Locate every Plasmodium falciparum-infected red blood cell.
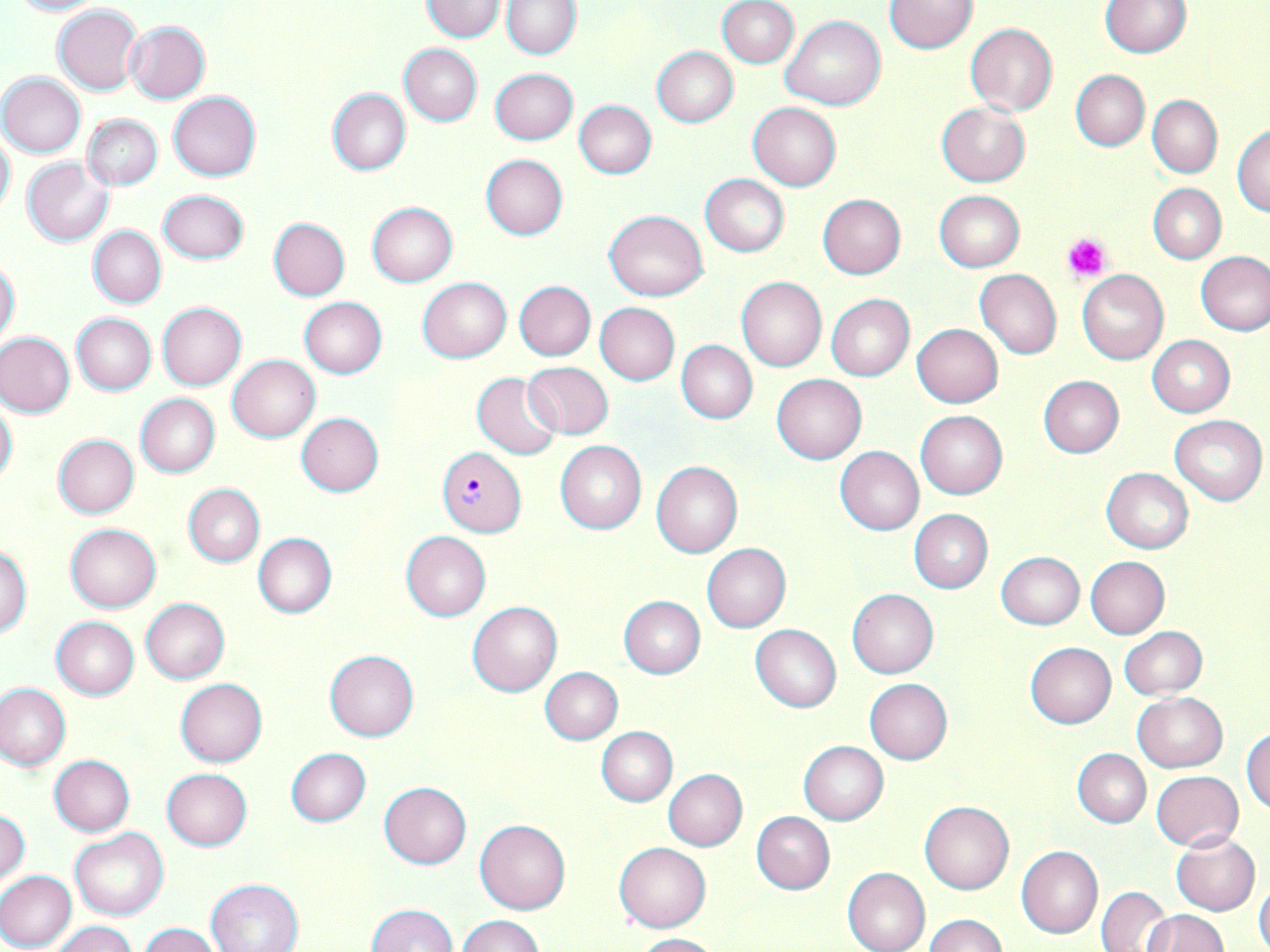
Approximate bounding boxes as (x1, y1, x2, y2) in pixels.
Plasmodium falciparum-infected red blood cells: (436, 447, 527, 535).

slide-level diagnosis = Plasmodium falciparum
stain = May-Grünwald-Giemsa
platelet locations = approximate bounding boxes as (x1, y1, x2, y2) in pixels: (1062, 232, 1111, 284)
image size = 1270×952 pixels
magnification = 1000x
preparation = thin blood smear
field of view = single
uninfected red blood cell locations = approximate bounding boxes as (x1, y1, x2, y2) in pixels: (421, 0, 506, 42), (8, 1, 104, 18), (501, 1, 581, 59), (716, 1, 798, 68), (885, 1, 978, 53), (1100, 1, 1191, 57), (52, 5, 142, 95), (781, 15, 886, 110), (123, 20, 211, 103), (965, 22, 1058, 116), (399, 44, 482, 125), (651, 46, 738, 127), (490, 68, 577, 145), (1071, 70, 1149, 151), (0, 72, 86, 157), (326, 87, 410, 176), (168, 91, 261, 181), (1148, 95, 1222, 177), (573, 99, 657, 179), (747, 102, 841, 191), (937, 102, 1029, 186), (81, 114, 163, 191), (1232, 123, 1270, 216), (0, 131, 16, 216), (480, 154, 568, 239), (22, 157, 113, 247), (700, 174, 789, 256), (1148, 183, 1225, 263), (158, 189, 248, 264), (934, 190, 1025, 271), (818, 194, 906, 279), (366, 202, 458, 286), (603, 209, 709, 300), (268, 217, 350, 301), (88, 226, 166, 308), (1196, 250, 1270, 336), (0, 259, 21, 347), (975, 270, 1062, 358), (1076, 270, 1168, 365), (736, 276, 827, 371), (417, 277, 511, 362), (514, 280, 595, 360), (826, 295, 914, 381), (299, 297, 387, 378), (157, 302, 246, 389), (595, 303, 680, 385), (71, 313, 156, 394), (912, 324, 1003, 407), (0, 332, 75, 417), (1148, 335, 1235, 417), (676, 340, 758, 423), (228, 355, 319, 441), (522, 361, 614, 439), (471, 371, 564, 460), (772, 374, 866, 463), (1038, 375, 1123, 458), (136, 394, 220, 477), (0, 397, 18, 487), (915, 409, 1008, 499), (295, 413, 383, 496), (1169, 415, 1267, 505), (51, 433, 139, 518), (555, 440, 647, 534), (834, 446, 924, 535), (652, 460, 743, 558), (1101, 468, 1193, 554), (184, 484, 264, 567), (909, 510, 993, 593), (65, 523, 161, 612), (401, 531, 490, 621), (253, 532, 337, 617), (702, 543, 790, 632), (0, 544, 32, 637), (996, 552, 1084, 629), (1085, 557, 1170, 639), (848, 589, 938, 678), (619, 596, 705, 678), (140, 598, 230, 683), (467, 601, 562, 696), (51, 617, 139, 699), (751, 624, 841, 713), (1120, 626, 1208, 699), (1025, 642, 1116, 727), (324, 650, 419, 742), (540, 666, 623, 744), (175, 679, 267, 767), (865, 679, 953, 764), (0, 682, 72, 769), (1132, 692, 1227, 773), (1242, 726, 1270, 815), (597, 727, 677, 806), (799, 741, 888, 824), (285, 748, 371, 826), (1072, 748, 1151, 827), (49, 754, 135, 837), (161, 768, 252, 850), (662, 769, 747, 851), (1151, 770, 1242, 851), (379, 782, 471, 868), (919, 801, 1014, 894), (1, 809, 30, 890), (751, 811, 834, 894), (475, 820, 570, 914), (70, 828, 169, 921), (1171, 831, 1260, 915), (614, 842, 711, 932), (1017, 846, 1102, 938), (842, 867, 930, 952), (0, 871, 77, 951), (1254, 875, 1270, 951), (205, 878, 303, 952), (1097, 886, 1170, 951), (366, 904, 456, 952), (1142, 910, 1227, 952), (924, 914, 1006, 952), (457, 915, 547, 952), (52, 921, 136, 952), (139, 923, 221, 952), (632, 933, 719, 952)
modality = light microscopy